Report the malaria status of this cell.
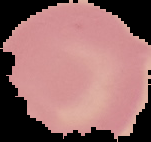
It is uninfected.

{
  "preparation": "thin blood film",
  "image_type": "cell region segmented out of the field of view; surrounding area masked to black",
  "image_size": "151×142 pixels"
}